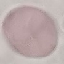

Summary:
  - Result: no malaria parasites detected
  - Stain: Giemsa
  - Capture: smartphone through the microscope eyepiece
  - Image type: automatically extracted cell patch, resized to 64 × 64 pixels
  - Preparation: thin blood film